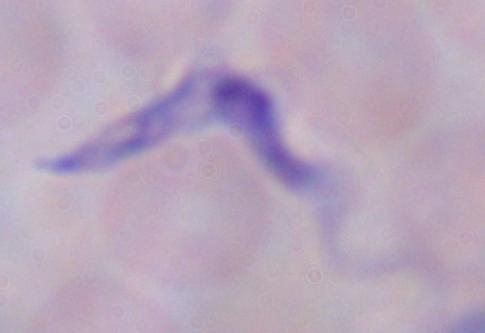
1000x magnification. A trypanosome is shown. Micrograph.